Locate platelets.
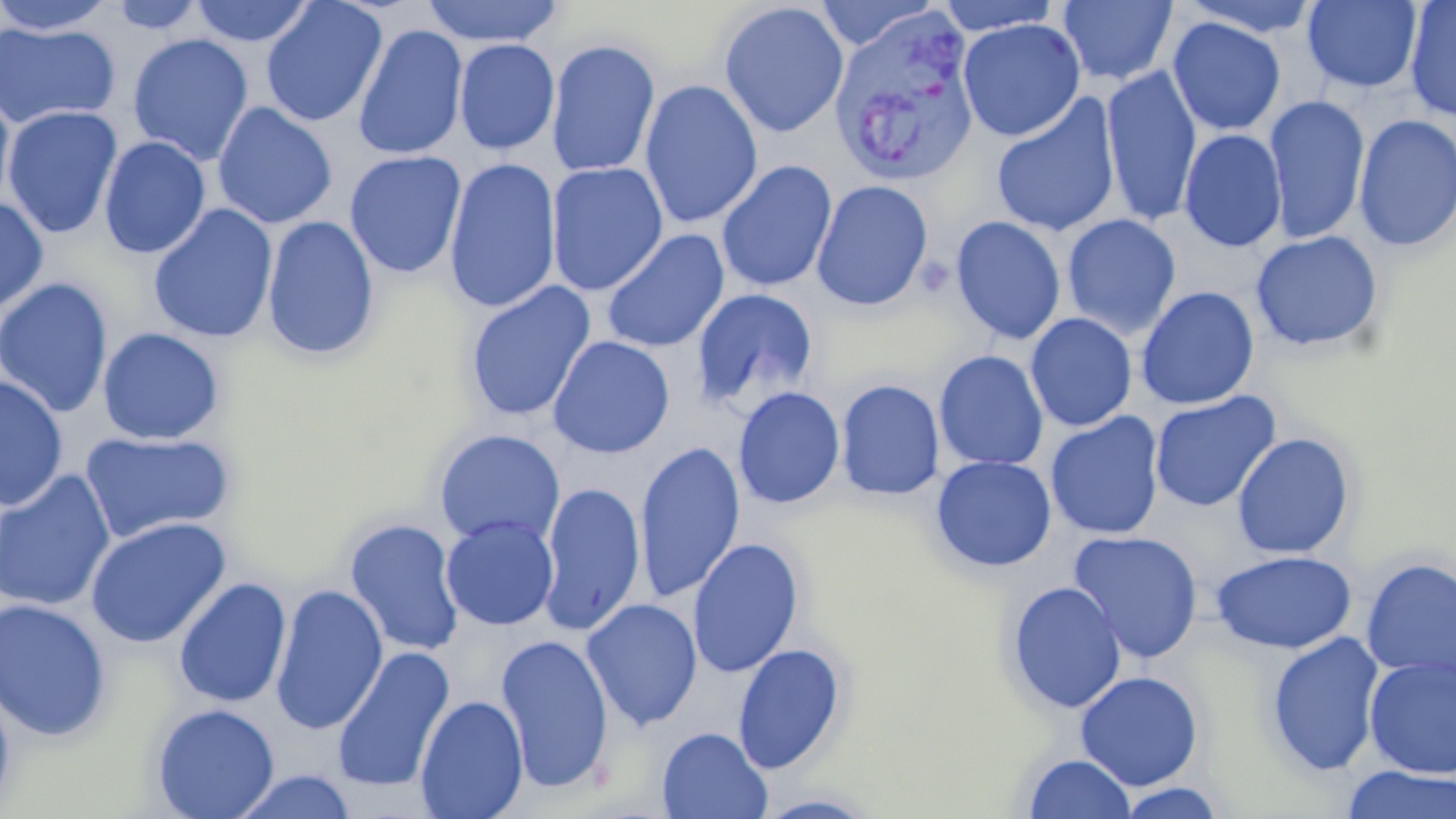

Approximate bounding boxes as named x1/y1/x2/y2 corners in pixels.
Platelets: (x1=915, y1=258, x2=955, y2=299).

Uninfected red blood cell locations: (x1=0, y1=0, x2=118, y2=35), (x1=188, y1=0, x2=315, y2=47), (x1=420, y1=0, x2=564, y2=47), (x1=933, y1=0, x2=1064, y2=35), (x1=1058, y1=0, x2=1177, y2=86), (x1=1179, y1=0, x2=1323, y2=38), (x1=105, y1=1, x2=208, y2=34), (x1=260, y1=1, x2=387, y2=127), (x1=813, y1=1, x2=937, y2=52), (x1=1302, y1=1, x2=1422, y2=93), (x1=1404, y1=1, x2=1456, y2=122), (x1=718, y1=2, x2=849, y2=138), (x1=1167, y1=17, x2=1286, y2=136), (x1=957, y1=18, x2=1085, y2=141), (x1=0, y1=22, x2=121, y2=130), (x1=353, y1=23, x2=468, y2=161), (x1=126, y1=33, x2=254, y2=166), (x1=453, y1=38, x2=560, y2=155), (x1=546, y1=38, x2=661, y2=177), (x1=1100, y1=65, x2=1202, y2=228), (x1=640, y1=79, x2=763, y2=230), (x1=0, y1=87, x2=16, y2=211), (x1=991, y1=95, x2=1120, y2=238), (x1=1264, y1=95, x2=1371, y2=246), (x1=211, y1=101, x2=338, y2=229), (x1=2, y1=105, x2=123, y2=239), (x1=1353, y1=114, x2=1456, y2=254), (x1=1179, y1=129, x2=1287, y2=252), (x1=98, y1=135, x2=211, y2=259), (x1=344, y1=150, x2=466, y2=278), (x1=443, y1=157, x2=561, y2=314), (x1=716, y1=160, x2=837, y2=293), (x1=546, y1=161, x2=668, y2=296), (x1=811, y1=179, x2=933, y2=311), (x1=0, y1=195, x2=49, y2=315), (x1=147, y1=203, x2=278, y2=343), (x1=262, y1=214, x2=380, y2=360), (x1=1062, y1=214, x2=1181, y2=339), (x1=950, y1=215, x2=1066, y2=345), (x1=600, y1=228, x2=729, y2=353), (x1=1250, y1=230, x2=1385, y2=353), (x1=0, y1=276, x2=114, y2=419), (x1=463, y1=280, x2=596, y2=423), (x1=1136, y1=286, x2=1259, y2=410), (x1=691, y1=287, x2=819, y2=411), (x1=1026, y1=309, x2=1258, y2=422), (x1=1025, y1=313, x2=1138, y2=432), (x1=97, y1=327, x2=225, y2=445), (x1=548, y1=335, x2=675, y2=459), (x1=934, y1=350, x2=1049, y2=471), (x1=0, y1=374, x2=69, y2=512), (x1=835, y1=378, x2=945, y2=500), (x1=733, y1=386, x2=845, y2=509), (x1=1149, y1=391, x2=1281, y2=512), (x1=1045, y1=411, x2=1165, y2=541), (x1=433, y1=428, x2=565, y2=549), (x1=79, y1=430, x2=235, y2=545), (x1=1231, y1=432, x2=1355, y2=560), (x1=634, y1=440, x2=745, y2=605), (x1=931, y1=455, x2=1057, y2=573), (x1=0, y1=469, x2=116, y2=612), (x1=540, y1=480, x2=645, y2=636), (x1=85, y1=515, x2=231, y2=649), (x1=441, y1=515, x2=559, y2=631), (x1=343, y1=517, x2=465, y2=657), (x1=1067, y1=530, x2=1204, y2=664), (x1=687, y1=537, x2=804, y2=678), (x1=1209, y1=550, x2=1357, y2=654), (x1=1360, y1=557, x2=1456, y2=683), (x1=173, y1=576, x2=292, y2=709), (x1=1005, y1=580, x2=1127, y2=714), (x1=269, y1=583, x2=388, y2=735), (x1=0, y1=597, x2=113, y2=742), (x1=581, y1=598, x2=703, y2=731), (x1=496, y1=632, x2=614, y2=792), (x1=1265, y1=632, x2=1385, y2=777), (x1=732, y1=642, x2=847, y2=775), (x1=331, y1=646, x2=454, y2=793), (x1=1363, y1=655, x2=1456, y2=778), (x1=1075, y1=670, x2=1204, y2=791), (x1=0, y1=686, x2=16, y2=815), (x1=415, y1=695, x2=528, y2=819), (x1=150, y1=703, x2=280, y2=819), (x1=657, y1=727, x2=773, y2=819), (x1=1022, y1=753, x2=1136, y2=818), (x1=1340, y1=765, x2=1456, y2=819), (x1=232, y1=770, x2=358, y2=818), (x1=1111, y1=781, x2=1228, y2=818), (x1=751, y1=792, x2=881, y2=819). Plasmodium vivax-infected red blood cell locations: (x1=827, y1=5, x2=981, y2=188). Slide-level diagnosis: Plasmodium vivax. May-Grünwald-Giemsa-stained preparation. Thin blood film. Image is 1456×819 pixels. Light microscopy. 1000x magnification. Single field of view.